Report the malaria status of this cell.
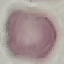
It is uninfected.

Cell patch, automatically extracted from a larger field of view and resized to 64 × 64 pixels. Thin smear of blood. Giemsa stain. Acquired by smartphone through the microscope eyepiece.